Look for Plasmodium parasites.
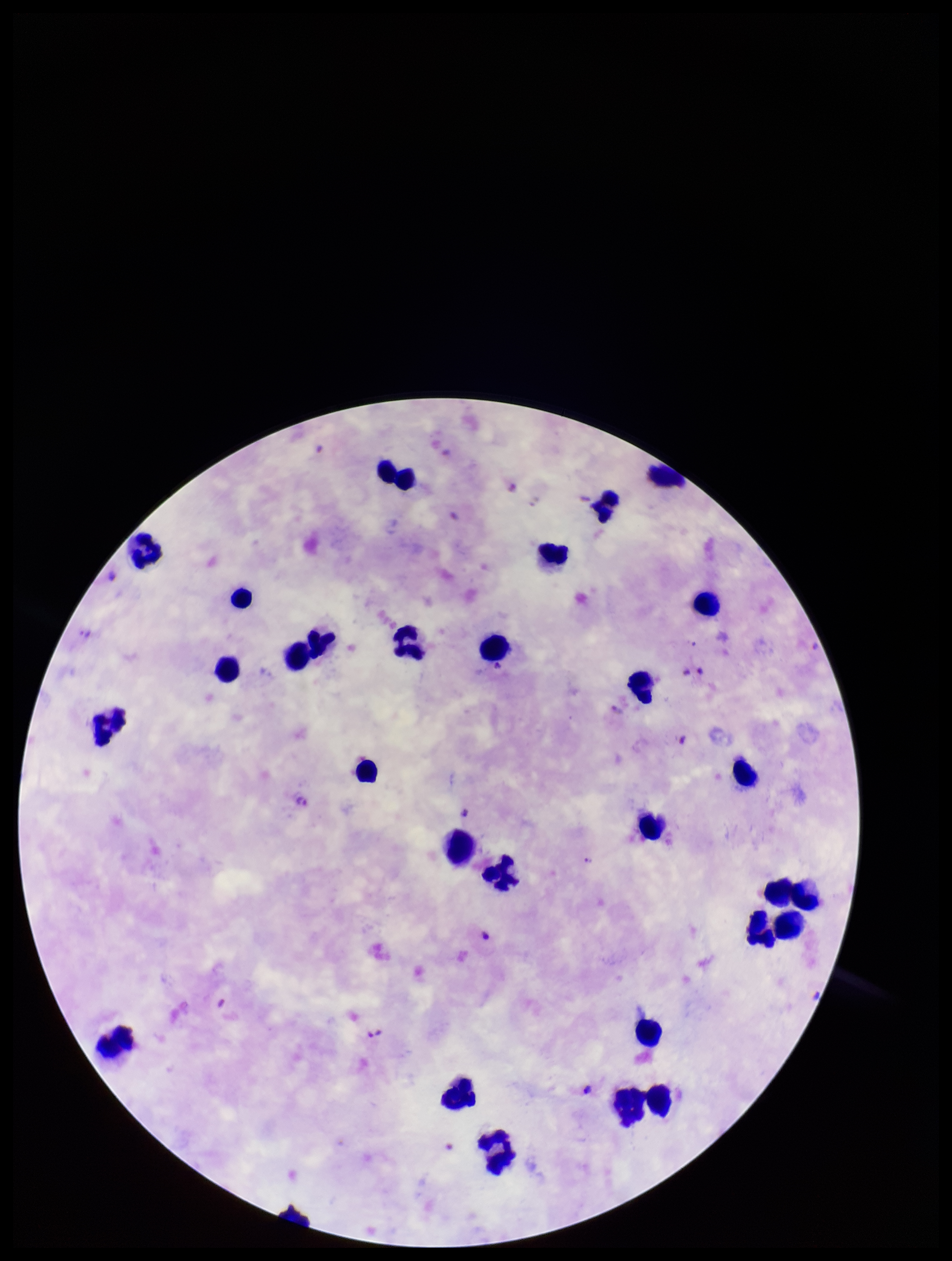

Identified.

patient_malaria_status: positive
leukocyte_count: 32
image_size: 952×1261 pixels
species_reported_for_this_patient: Plasmodium falciparum
field_of_view: one from this slide
capture: smartphone photograph through the microscope eyepiece
parasite_count: 4
stain: Giemsa
preparation: thick blood smear